Identify the blood parasite species.
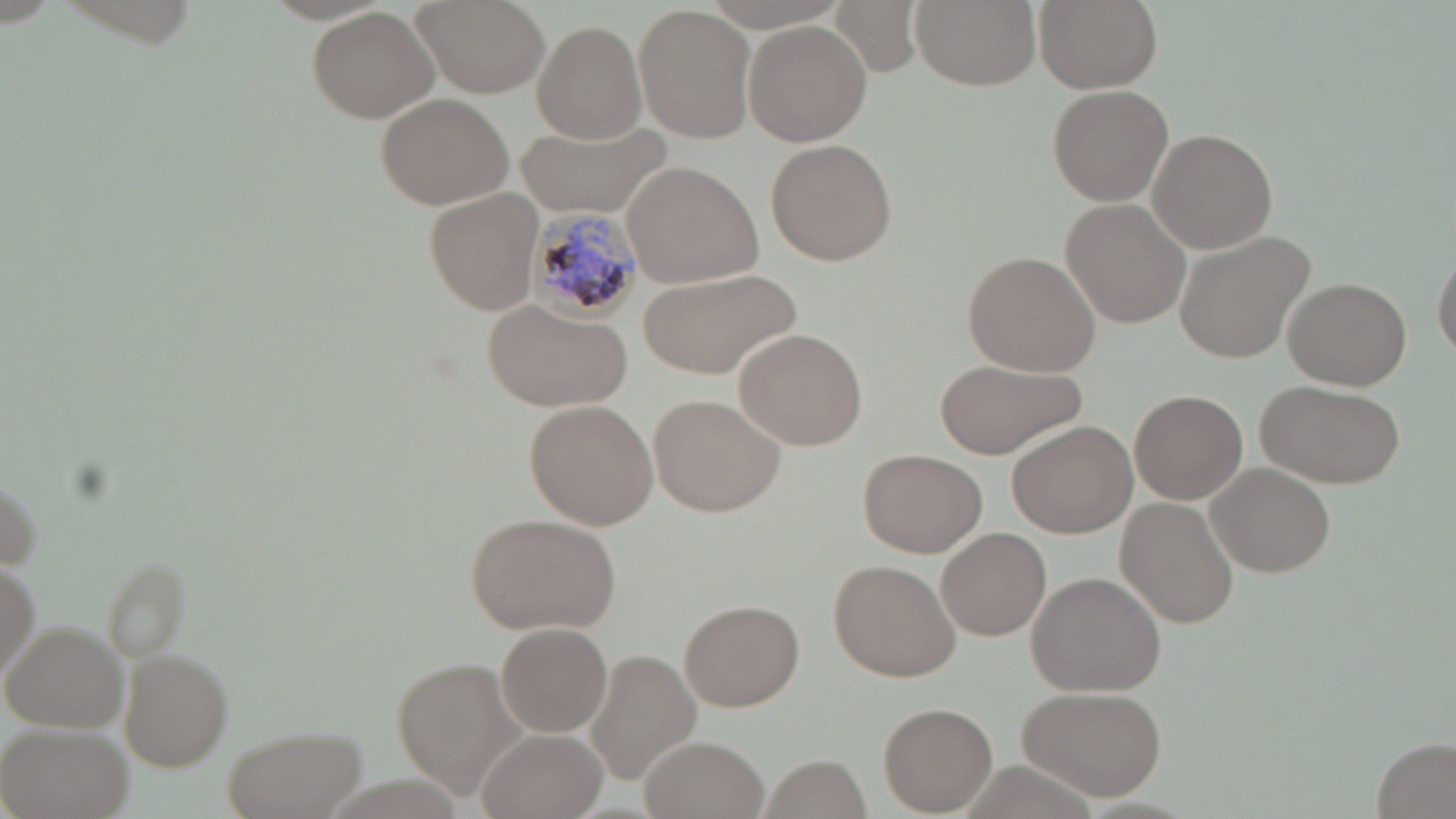
Plasmodium malariae.

Approximate bounding boxes as named x1/y1/x2/y2 corners in pixels. Plasmodium malariae-infected red blood cell locations: (x1=528, y1=208, x2=648, y2=320). Uninfected red blood cell locations: (x1=411, y1=0, x2=548, y2=99), (x1=830, y1=0, x2=929, y2=77), (x1=909, y1=0, x2=1041, y2=91), (x1=1036, y1=0, x2=1164, y2=95), (x1=306, y1=5, x2=443, y2=126), (x1=634, y1=6, x2=758, y2=144), (x1=744, y1=19, x2=872, y2=147), (x1=531, y1=20, x2=647, y2=145), (x1=1046, y1=83, x2=1173, y2=207), (x1=374, y1=92, x2=514, y2=211), (x1=515, y1=116, x2=670, y2=218), (x1=1147, y1=129, x2=1278, y2=253), (x1=765, y1=139, x2=897, y2=265), (x1=617, y1=160, x2=766, y2=287), (x1=426, y1=189, x2=544, y2=315), (x1=1058, y1=199, x2=1191, y2=329), (x1=1174, y1=228, x2=1318, y2=364), (x1=962, y1=250, x2=1101, y2=377), (x1=1431, y1=252, x2=1455, y2=361), (x1=635, y1=268, x2=802, y2=382), (x1=1279, y1=278, x2=1413, y2=389), (x1=485, y1=300, x2=632, y2=411), (x1=733, y1=328, x2=868, y2=450), (x1=933, y1=357, x2=1086, y2=460), (x1=1257, y1=379, x2=1404, y2=487), (x1=1131, y1=390, x2=1248, y2=504), (x1=649, y1=393, x2=786, y2=518), (x1=526, y1=398, x2=661, y2=530), (x1=1007, y1=420, x2=1136, y2=539), (x1=858, y1=447, x2=985, y2=558), (x1=1205, y1=463, x2=1336, y2=577), (x1=1114, y1=498, x2=1239, y2=629), (x1=462, y1=511, x2=623, y2=636), (x1=936, y1=527, x2=1050, y2=641), (x1=97, y1=555, x2=194, y2=663), (x1=1, y1=558, x2=41, y2=686), (x1=830, y1=559, x2=962, y2=682), (x1=1028, y1=570, x2=1168, y2=697), (x1=679, y1=598, x2=804, y2=711), (x1=3, y1=620, x2=129, y2=733), (x1=496, y1=621, x2=613, y2=738), (x1=118, y1=649, x2=234, y2=770), (x1=586, y1=650, x2=699, y2=783), (x1=390, y1=659, x2=531, y2=798), (x1=1020, y1=683, x2=1167, y2=803), (x1=879, y1=702, x2=997, y2=816), (x1=0, y1=721, x2=133, y2=819), (x1=227, y1=723, x2=370, y2=819), (x1=474, y1=729, x2=606, y2=819), (x1=640, y1=734, x2=766, y2=818), (x1=1372, y1=739, x2=1454, y2=818), (x1=761, y1=757, x2=870, y2=816). May-Grünwald-Giemsa-stained preparation. Single field of view. Captured at 1000x magnification. Light microscopy. Thin blood film. Image is 1456×819 pixels.